Give the extent of all uninfected red blood cells.
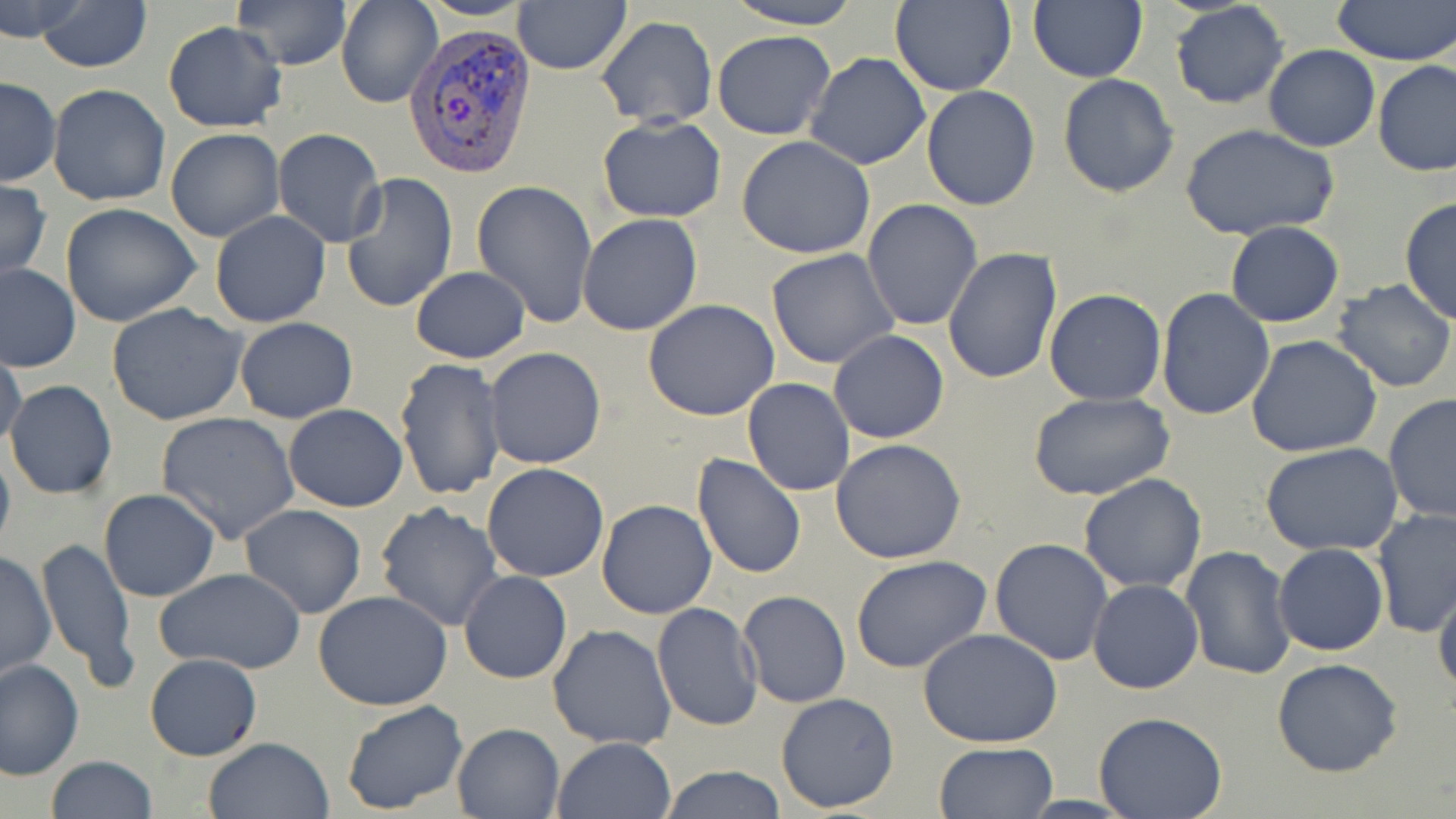

Approximate bounding boxes as named x1/y1/x2/y2 corners in pixels.
Uninfected red blood cells: (x1=0, y1=0, x2=84, y2=40), (x1=32, y1=0, x2=153, y2=72), (x1=231, y1=0, x2=351, y2=71), (x1=720, y1=0, x2=864, y2=29), (x1=891, y1=0, x2=1018, y2=97), (x1=1028, y1=0, x2=1146, y2=82), (x1=1333, y1=0, x2=1456, y2=67), (x1=336, y1=1, x2=440, y2=109), (x1=1170, y1=1, x2=1291, y2=110), (x1=513, y1=2, x2=632, y2=75), (x1=596, y1=16, x2=716, y2=128), (x1=162, y1=20, x2=287, y2=132), (x1=712, y1=31, x2=836, y2=140), (x1=1263, y1=45, x2=1379, y2=151), (x1=805, y1=53, x2=930, y2=171), (x1=1372, y1=60, x2=1455, y2=177), (x1=1057, y1=73, x2=1181, y2=196), (x1=0, y1=77, x2=61, y2=187), (x1=47, y1=83, x2=172, y2=207), (x1=920, y1=85, x2=1041, y2=211), (x1=596, y1=116, x2=728, y2=221), (x1=1178, y1=122, x2=1340, y2=240), (x1=165, y1=127, x2=284, y2=242), (x1=272, y1=128, x2=386, y2=247), (x1=736, y1=136, x2=878, y2=259), (x1=339, y1=171, x2=459, y2=315), (x1=0, y1=178, x2=51, y2=283), (x1=473, y1=182, x2=599, y2=327), (x1=1399, y1=196, x2=1456, y2=325), (x1=861, y1=199, x2=983, y2=331), (x1=60, y1=202, x2=202, y2=327), (x1=209, y1=211, x2=331, y2=327), (x1=577, y1=214, x2=704, y2=335), (x1=866, y1=216, x2=1056, y2=365), (x1=1224, y1=220, x2=1344, y2=328), (x1=943, y1=247, x2=1062, y2=385), (x1=766, y1=248, x2=899, y2=369), (x1=0, y1=262, x2=81, y2=372), (x1=409, y1=267, x2=532, y2=363), (x1=1330, y1=278, x2=1456, y2=393), (x1=1154, y1=287, x2=1275, y2=421), (x1=1044, y1=288, x2=1166, y2=405), (x1=644, y1=300, x2=781, y2=421), (x1=107, y1=304, x2=250, y2=426), (x1=234, y1=317, x2=358, y2=423), (x1=828, y1=330, x2=949, y2=444), (x1=1246, y1=334, x2=1384, y2=458), (x1=0, y1=342, x2=27, y2=456), (x1=483, y1=347, x2=606, y2=470), (x1=394, y1=357, x2=507, y2=501), (x1=742, y1=378, x2=855, y2=496), (x1=4, y1=380, x2=116, y2=499), (x1=1028, y1=390, x2=1176, y2=502), (x1=1382, y1=393, x2=1456, y2=523), (x1=283, y1=404, x2=408, y2=512), (x1=155, y1=411, x2=300, y2=542), (x1=831, y1=439, x2=966, y2=564), (x1=0, y1=440, x2=15, y2=560), (x1=1262, y1=442, x2=1403, y2=557), (x1=691, y1=455, x2=807, y2=578), (x1=481, y1=462, x2=610, y2=583), (x1=1078, y1=473, x2=1207, y2=592), (x1=98, y1=489, x2=219, y2=602), (x1=596, y1=498, x2=718, y2=619), (x1=374, y1=502, x2=504, y2=632), (x1=238, y1=504, x2=366, y2=619), (x1=1372, y1=508, x2=1456, y2=640), (x1=35, y1=536, x2=139, y2=691), (x1=989, y1=538, x2=1113, y2=667), (x1=1273, y1=543, x2=1389, y2=656), (x1=1181, y1=545, x2=1297, y2=682), (x1=1, y1=549, x2=56, y2=680), (x1=851, y1=555, x2=993, y2=675), (x1=157, y1=568, x2=305, y2=675), (x1=458, y1=570, x2=572, y2=684), (x1=1087, y1=579, x2=1204, y2=694), (x1=1433, y1=579, x2=1456, y2=701), (x1=314, y1=591, x2=453, y2=711), (x1=738, y1=591, x2=851, y2=709), (x1=652, y1=602, x2=763, y2=732), (x1=548, y1=625, x2=677, y2=749), (x1=918, y1=628, x2=1064, y2=750), (x1=144, y1=653, x2=263, y2=761), (x1=1270, y1=657, x2=1403, y2=777), (x1=0, y1=659, x2=84, y2=780), (x1=774, y1=691, x2=901, y2=813), (x1=340, y1=699, x2=468, y2=815), (x1=1092, y1=712, x2=1226, y2=819), (x1=451, y1=723, x2=563, y2=817), (x1=203, y1=737, x2=333, y2=819), (x1=551, y1=737, x2=676, y2=819), (x1=932, y1=741, x2=1057, y2=818), (x1=45, y1=756, x2=159, y2=818), (x1=658, y1=766, x2=787, y2=818).

Plasmodium vivax-infected red blood cell locations: (x1=405, y1=22, x2=536, y2=183). Slide-level diagnosis: Plasmodium vivax. May-Grünwald-Giemsa stain. Captured at 1000x magnification. One field of a larger specimen. Thin blood film. Image is 1456×819 pixels. Optical microscopy.